Outline each blood parasite and name the species.
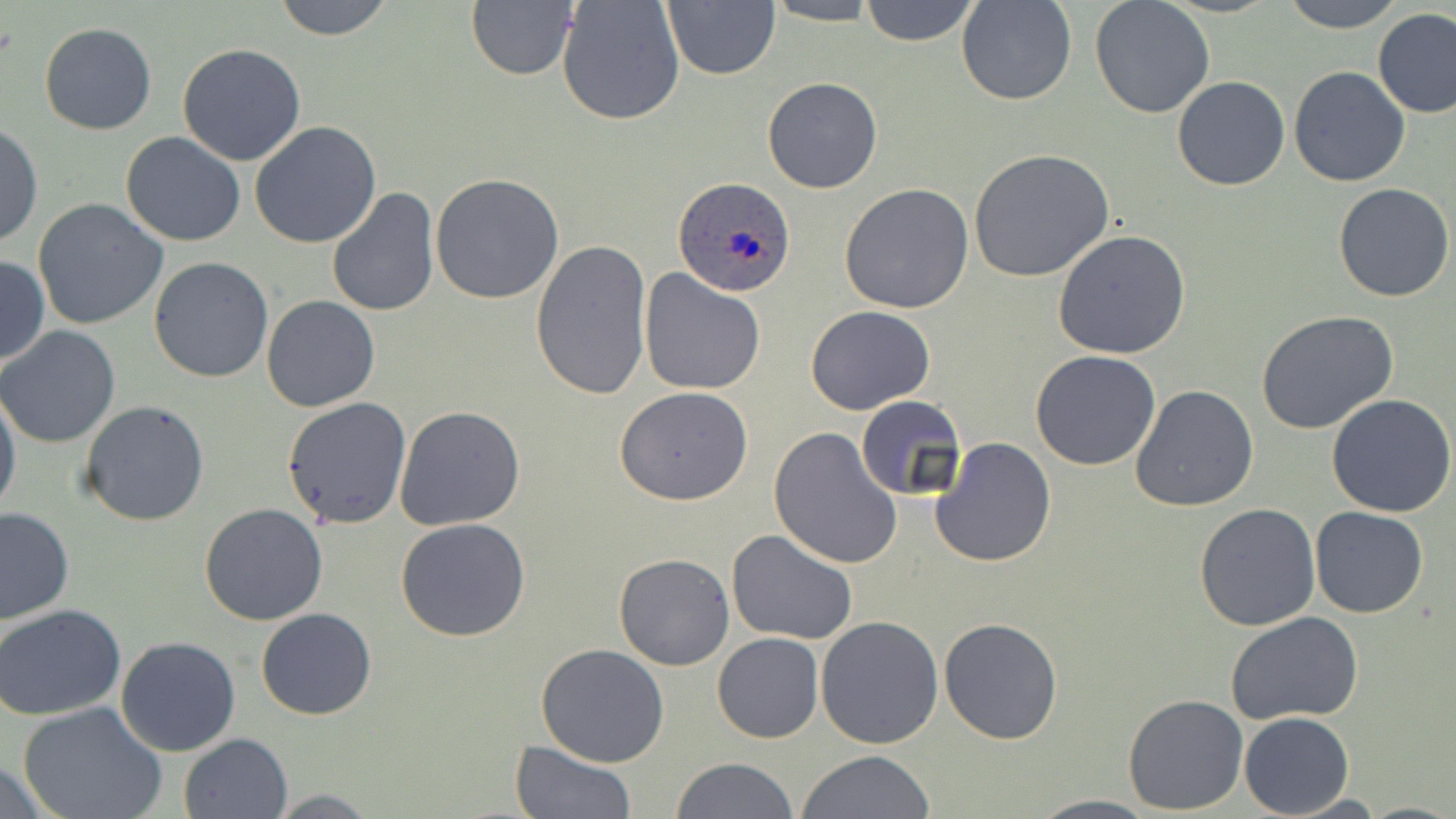
Approximate bounding boxes as named x1/y1/x2/y2 corners in pixels.
Plasmodium ovale-infected red blood cells: (x1=672, y1=177, x2=793, y2=297).
No Plasmodium falciparum, Plasmodium malariae, Plasmodium vivax, Babesia divergens, or Trypanosoma brucei observed.

Uninfected red blood cell locations: (x1=270, y1=0, x2=396, y2=41), (x1=556, y1=0, x2=685, y2=126), (x1=857, y1=0, x2=981, y2=47), (x1=956, y1=0, x2=1075, y2=106), (x1=1279, y1=0, x2=1405, y2=31), (x1=660, y1=1, x2=780, y2=81), (x1=763, y1=1, x2=883, y2=26), (x1=1089, y1=1, x2=1215, y2=119), (x1=465, y1=2, x2=577, y2=81), (x1=1374, y1=9, x2=1456, y2=118), (x1=39, y1=22, x2=157, y2=135), (x1=176, y1=43, x2=306, y2=166), (x1=1288, y1=65, x2=1411, y2=186), (x1=1172, y1=75, x2=1290, y2=191), (x1=762, y1=76, x2=882, y2=194), (x1=1, y1=121, x2=42, y2=249), (x1=250, y1=121, x2=382, y2=249), (x1=121, y1=130, x2=245, y2=247), (x1=970, y1=149, x2=1115, y2=284), (x1=430, y1=173, x2=566, y2=305), (x1=839, y1=182, x2=974, y2=315), (x1=1333, y1=182, x2=1454, y2=301), (x1=326, y1=187, x2=441, y2=318), (x1=32, y1=197, x2=167, y2=331), (x1=1053, y1=229, x2=1190, y2=359), (x1=530, y1=239, x2=651, y2=400), (x1=0, y1=255, x2=48, y2=367), (x1=149, y1=257, x2=274, y2=383), (x1=638, y1=268, x2=765, y2=395), (x1=262, y1=295, x2=381, y2=412), (x1=806, y1=304, x2=935, y2=415), (x1=1256, y1=311, x2=1398, y2=434), (x1=0, y1=326, x2=122, y2=448), (x1=1031, y1=349, x2=1161, y2=470), (x1=1130, y1=385, x2=1259, y2=513), (x1=614, y1=386, x2=753, y2=505), (x1=0, y1=387, x2=21, y2=522), (x1=1327, y1=394, x2=1456, y2=517), (x1=282, y1=397, x2=413, y2=529), (x1=855, y1=398, x2=968, y2=505), (x1=78, y1=400, x2=210, y2=526), (x1=394, y1=406, x2=525, y2=530), (x1=769, y1=426, x2=903, y2=570), (x1=931, y1=438, x2=1056, y2=569), (x1=1194, y1=502, x2=1322, y2=632), (x1=198, y1=503, x2=329, y2=626), (x1=1309, y1=506, x2=1430, y2=618), (x1=1, y1=507, x2=74, y2=626), (x1=395, y1=518, x2=530, y2=641), (x1=726, y1=530, x2=858, y2=644), (x1=614, y1=553, x2=734, y2=671), (x1=0, y1=604, x2=126, y2=719), (x1=255, y1=608, x2=378, y2=720), (x1=1227, y1=612, x2=1365, y2=725), (x1=816, y1=616, x2=944, y2=749), (x1=939, y1=618, x2=1063, y2=745), (x1=713, y1=633, x2=823, y2=743), (x1=114, y1=637, x2=240, y2=757), (x1=535, y1=643, x2=670, y2=768), (x1=1123, y1=693, x2=1249, y2=815), (x1=19, y1=704, x2=168, y2=819), (x1=1239, y1=712, x2=1355, y2=818), (x1=179, y1=732, x2=293, y2=818), (x1=511, y1=742, x2=635, y2=819), (x1=797, y1=748, x2=936, y2=818), (x1=0, y1=758, x2=59, y2=817), (x1=672, y1=758, x2=799, y2=818), (x1=1283, y1=793, x2=1395, y2=818), (x1=1026, y1=794, x2=1160, y2=818). Slide-level diagnosis: Plasmodium ovale. Single field of view. Captured at 1000x magnification. May-Grünwald-Giemsa stain. Thin blood film. Image is 1456×819 pixels. Optical microscopy.